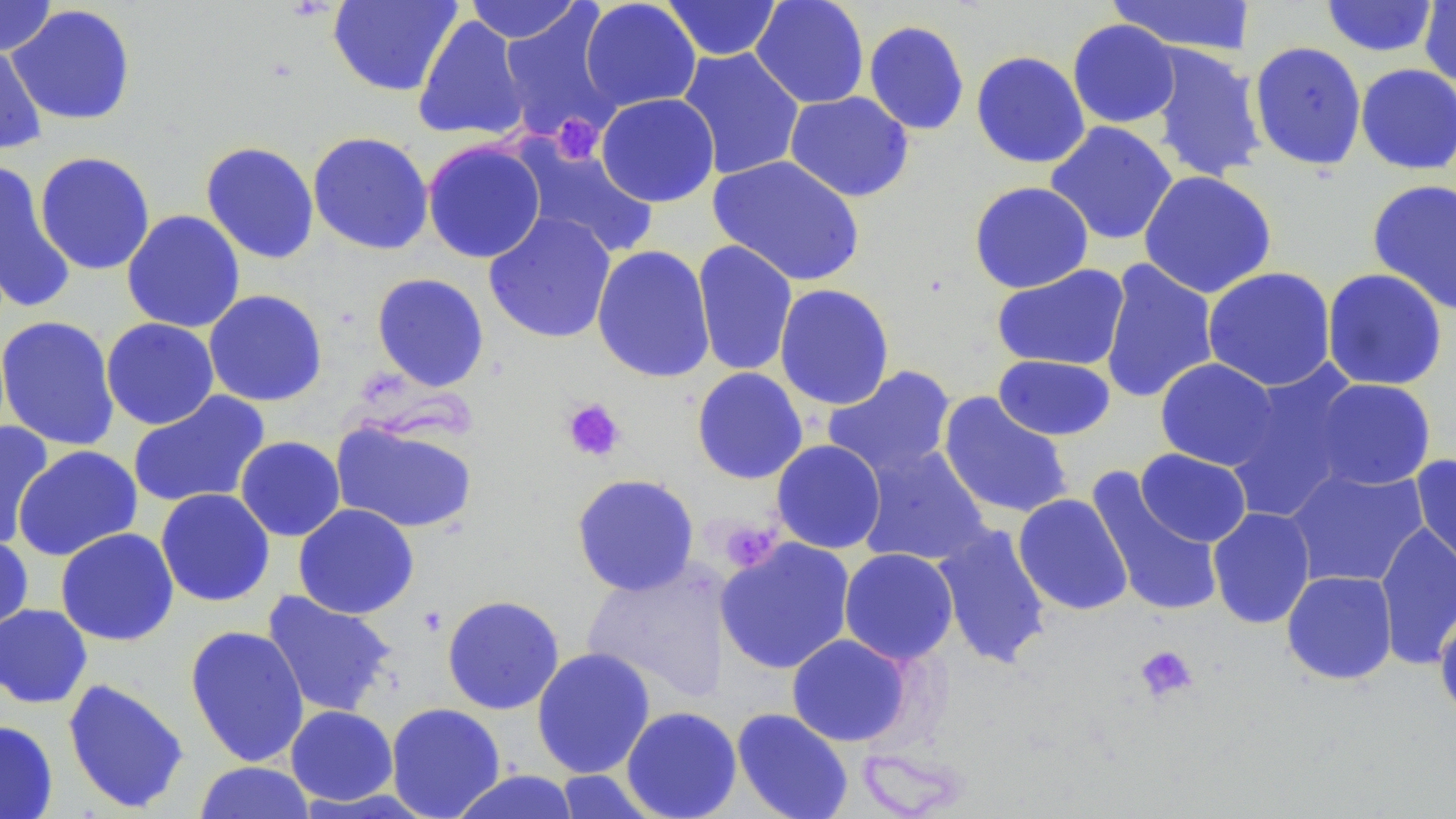 Approximate bounding boxes as (x1,y1)-(x2,y2) corner pairs in pixels. Uninfected red blood cell locations: (0,0)-(57,56), (328,0)-(462,97), (464,0)-(584,43), (580,0)-(701,111), (662,0)-(783,61), (750,0)-(870,109), (1107,0)-(1256,56), (1320,0)-(1439,57), (1418,0)-(1456,89), (6,5)-(136,126), (496,6)-(624,143), (412,15)-(529,142), (1067,19)-(1180,128), (863,20)-(970,136), (1248,41)-(1367,170), (0,44)-(47,155), (1145,44)-(1267,182), (676,47)-(806,181), (971,50)-(1090,169), (1355,63)-(1456,175), (784,91)-(914,202), (596,92)-(720,207), (1045,121)-(1179,246), (307,131)-(434,255), (423,140)-(546,264), (513,140)-(658,259), (200,141)-(320,264), (34,151)-(156,275), (707,155)-(866,287), (0,162)-(77,313), (1138,170)-(1277,298), (1366,178)-(1456,316), (969,181)-(1094,293), (122,209)-(246,333), (483,212)-(617,344), (692,240)-(798,377), (591,245)-(716,384), (1098,259)-(1219,404), (991,264)-(1130,371), (1202,267)-(1337,391), (1321,268)-(1448,391), (371,273)-(490,392), (774,283)-(895,410), (203,289)-(328,407), (0,315)-(120,451), (101,317)-(220,429), (993,355)-(1116,440), (1154,358)-(1280,471), (1222,363)-(1366,524), (823,364)-(957,480), (691,367)-(808,484), (1309,378)-(1437,491), (127,390)-(271,509), (937,392)-(1074,520), (330,418)-(479,533), (0,421)-(55,549), (235,436)-(346,542), (771,439)-(887,554), (12,445)-(143,561), (857,445)-(992,566), (1135,448)-(1252,547), (1410,454)-(1456,579), (1283,465)-(1429,589), (1085,468)-(1225,618), (571,473)-(700,596), (155,488)-(275,607), (1013,494)-(1132,615), (293,503)-(419,620), (1207,506)-(1316,629), (1374,521)-(1456,669), (933,523)-(1052,669), (55,527)-(180,646), (0,532)-(34,635), (715,537)-(856,674), (839,547)-(959,664), (582,560)-(729,704), (1281,570)-(1398,685), (260,590)-(397,718), (441,594)-(565,715), (0,603)-(92,709), (1434,606)-(1456,722), (184,625)-(310,767), (786,633)-(913,747), (531,647)-(656,778), (62,677)-(190,814), (386,702)-(506,818), (285,705)-(398,806), (621,706)-(742,819), (731,707)-(854,819), (0,719)-(58,818), (193,761)-(317,819), (449,769)-(582,819), (553,769)-(659,818). Platelet locations: (550,114)-(603,164), (561,397)-(626,462), (717,520)-(781,573), (1133,644)-(1198,704). Slide-level diagnosis: negative for blood parasites. Optical microscopy. May-Grünwald-Giemsa-stained preparation. Image is 1456×819 pixels. Thin blood film. Captured at 1000x magnification. Single field of view.